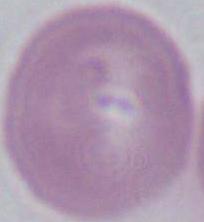
identification = red blood cell
modality = photomicrograph
magnification = 1000x